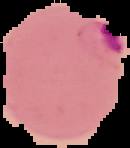
Image is 130×148 pixels. Result: Plasmodium parasites identified. Segmented cell region on a black background. From a thin blood smear.